Identify the preparation type.
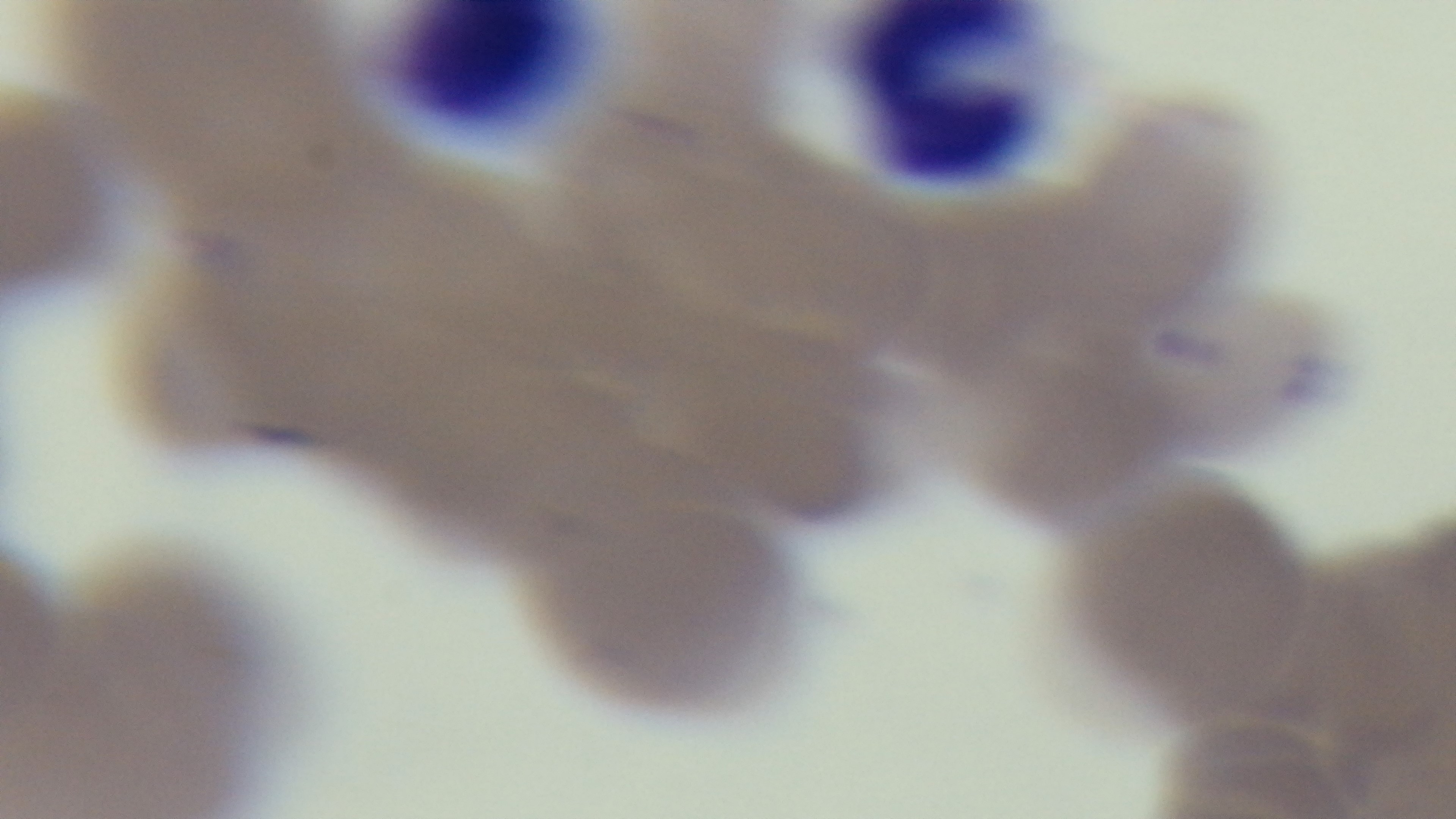
A thin smear.

Photomicrograph. Malaria status: positive. 100x oil-immersion objective. Giemsa-stained. Captured with a mounted 4K digital camera. One field from the slide.